Outline each blood parasite and name the species.
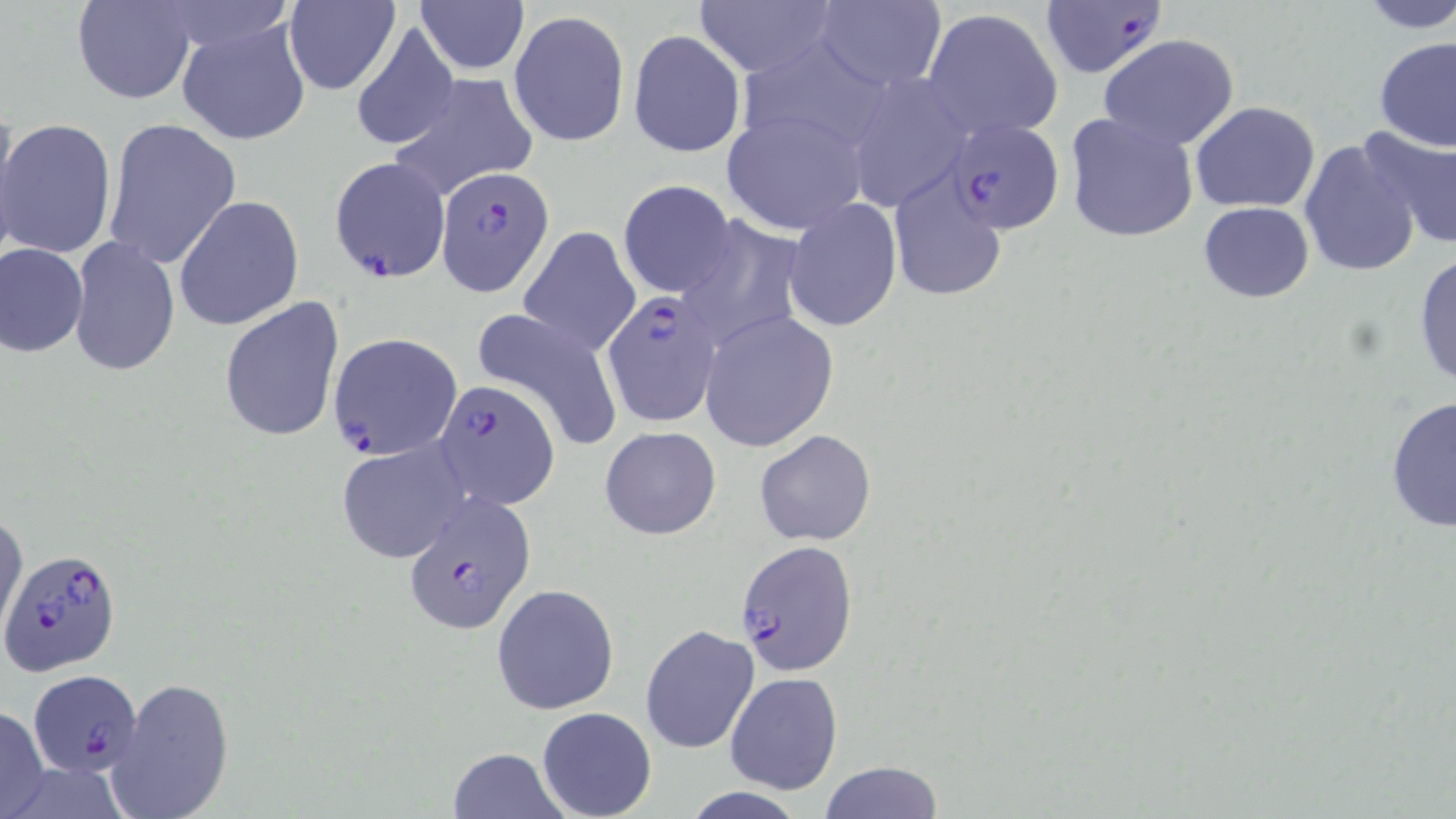
Approximate bounding boxes as (x1,y1)-(x2,y2) corner pairs in pixels.
Plasmodium falciparum-infected red blood cells: (1038,0)-(1168,81), (944,122)-(1064,235), (328,157)-(450,282), (436,167)-(554,296), (600,291)-(726,428), (326,333)-(462,462), (432,381)-(560,509), (403,498)-(536,635), (733,539)-(859,674), (4,548)-(120,676), (27,670)-(140,777).
No Plasmodium ovale, Plasmodium malariae, Plasmodium vivax, Babesia divergens, or Trypanosoma brucei observed.

Summary:
  - Uninfected red blood cell locations: (72,0)-(198,104), (414,0)-(529,73), (692,0)-(838,76), (1353,0)-(1456,33), (284,1)-(400,95), (812,1)-(947,91), (920,7)-(1064,142), (509,10)-(629,147), (178,17)-(311,148), (349,23)-(461,152), (628,28)-(746,159), (1097,34)-(1242,152), (1373,36)-(1456,152), (842,72)-(972,211), (387,73)-(538,201), (1190,101)-(1320,213), (721,110)-(867,236), (1065,112)-(1199,244), (102,117)-(242,272), (0,119)-(118,260), (1359,126)-(1456,252), (1297,138)-(1423,280), (888,170)-(1010,301), (617,179)-(736,298), (175,196)-(304,331), (1197,199)-(1316,302), (785,201)-(902,332), (677,216)-(808,357), (518,225)-(640,358), (68,237)-(180,378), (0,243)-(88,358), (1411,248)-(1456,389), (220,297)-(346,444), (470,305)-(625,453), (700,311)-(838,451), (1383,395)-(1456,534), (599,424)-(722,539), (755,428)-(875,545), (338,440)-(470,564), (0,508)-(27,644), (491,584)-(619,715), (640,623)-(759,754), (723,672)-(844,795), (106,675)-(236,819), (0,705)-(50,818), (537,707)-(656,819), (445,747)-(571,818), (818,760)-(945,818), (675,788)-(814,819)
  - Slide-level diagnosis: Plasmodium falciparum
  - Image size: 1456×819 pixels
  - Modality: light microscopy
  - Field of view: single
  - Preparation: thin blood smear
  - Stain: May-Grünwald-Giemsa
  - Magnification: 1000x